Report the malaria status of this cell.
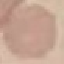
It is uninfected.

capture: smartphone camera at the microscope eyepiece
image_type: automatically extracted cell patch, resized to 64 × 64 pixels
preparation: thin blood smear
stain: Giemsa